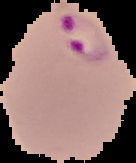
image size = 136×163 pixels
result = Plasmodium parasites detected
preparation = thin blood smear
image type = segmented cell region on a black background